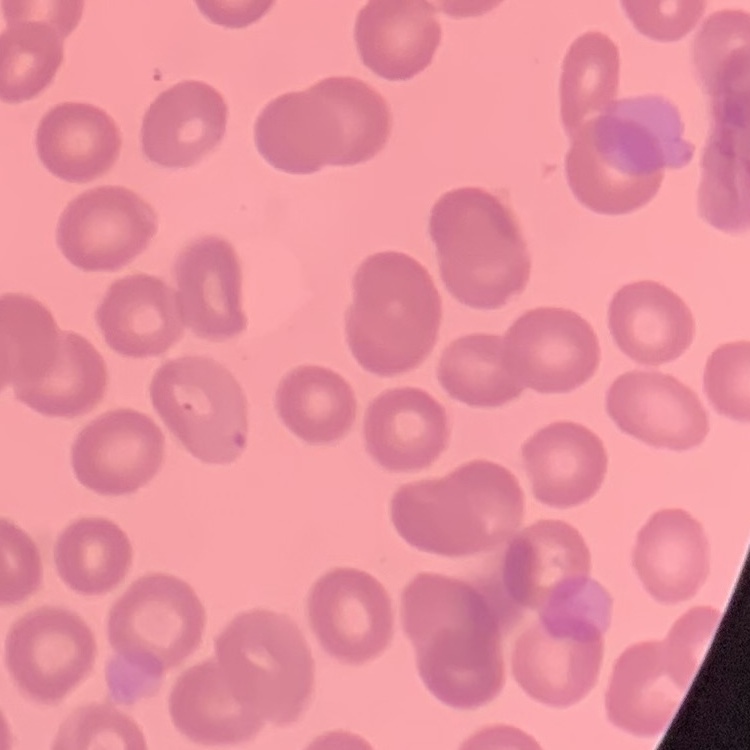 The erythrocytes exhibit no rouleaux formation. Stained with either Field's or Giemsa. One tile cut from a larger photomicrograph. Thin blood film.